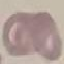 Result: no malaria parasites seen. Thin blood film. Cell patch, automatically extracted from a larger field of view and resized to 64 × 64 pixels. Photographed with a smartphone camera at the microscope eyepiece. Giemsa-stained preparation.